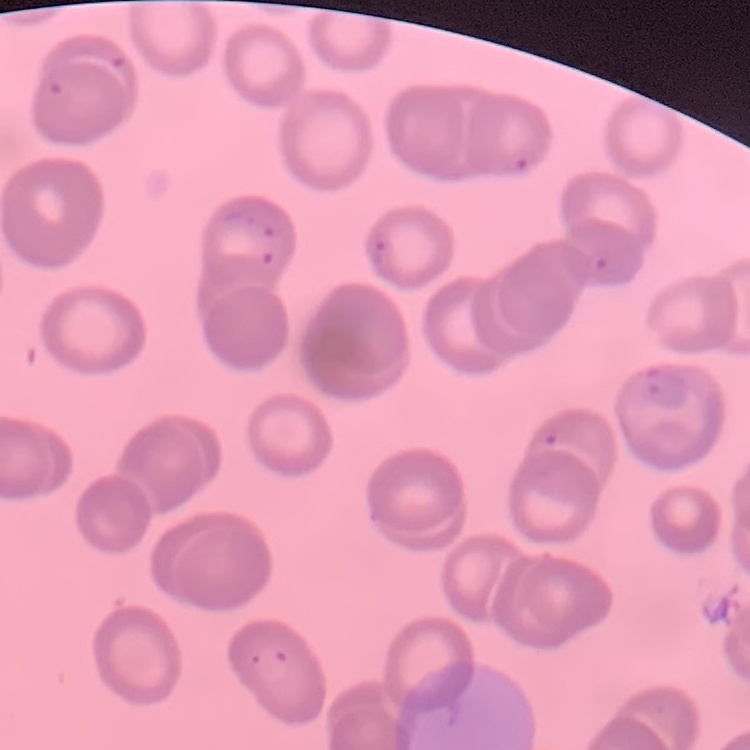
red blood cell morphology = no rouleaux formation
stain = Field's or Giemsa
preparation = thin peripheral smear
image type = one tile cut from a larger photomicrograph